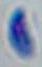
Toxoplasma gondii is seen. Photomicrograph. 1000x magnification.